Report the malaria status of this cell.
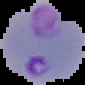
Parasitized.

image_type: cell region segmented out of the field of view; surrounding area masked to black
preparation: thin blood smear
image_size: 85×85 pixels